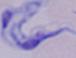

{
  "modality": "photomicrograph",
  "identification": "trypanosome",
  "magnification": "1000x"
}